Describe the morphology of the red blood cells.
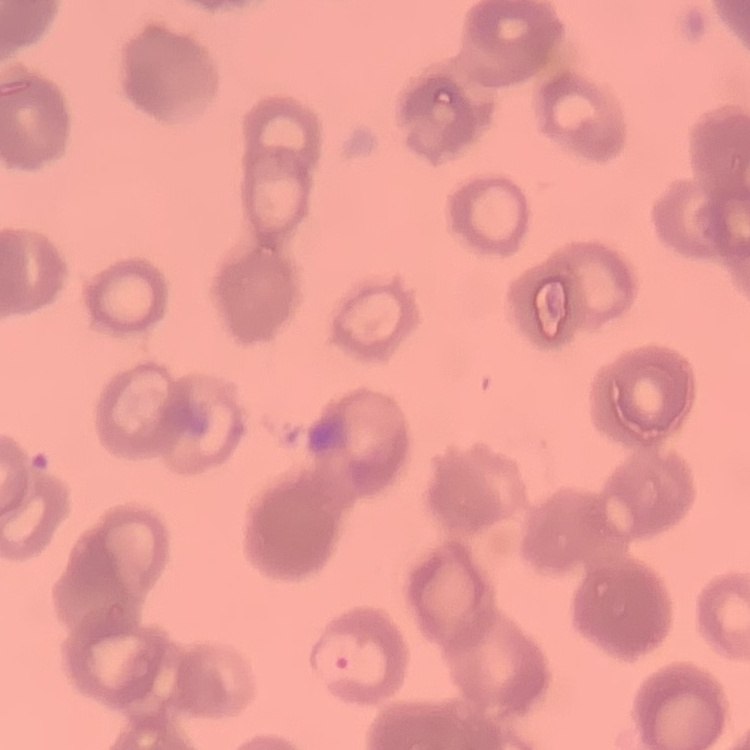
Rouleaux formation.

{
  "preparation": "thin peripheral smear",
  "stain": "Field's or Giemsa",
  "image_type": "square crop of a larger photomicrograph"
}